Assess this cell for malaria.
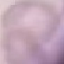

Uninfected.

stain = Giemsa
image type = cell patch, automatically extracted from a larger field of view and resized to 64 × 64 pixels
preparation = thin blood film
capture = smartphone through the microscope eyepiece